Assess this cell for malaria.
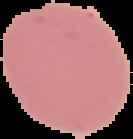
Uninfected.

preparation = thin blood film
image type = segmented cell region with the area outside set to black
image size = 133×139 pixels